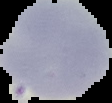

{
  "image_size": "112×103 pixels",
  "image_type": "segmented cell region on a black background",
  "malaria_status": "uninfected",
  "preparation": "thin blood smear"
}